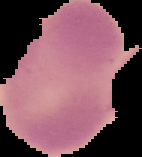

Image is 142×157 pixels. The area outside the segmented cell region is set to black. Malaria status: uninfected. From a thin blood film.